Point out Plasmodium parasites and leukocytes.
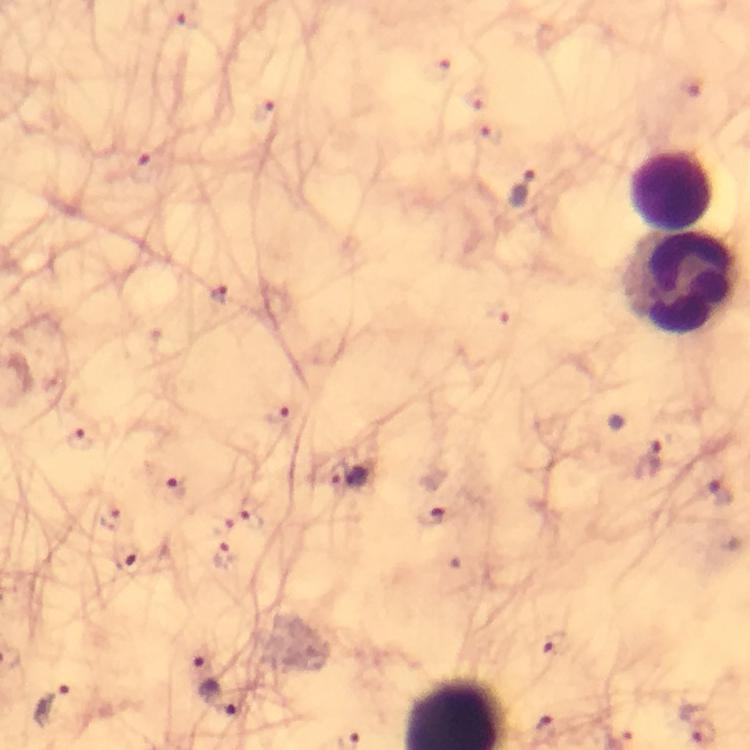
Approximate centers as (x, y) in pixels.
Plasmodium parasites: (440, 70), (692, 86), (478, 100), (262, 113), (493, 132), (140, 168), (522, 188), (218, 295), (280, 419), (79, 440), (651, 459), (333, 475), (356, 480), (173, 488), (716, 494), (250, 515), (431, 517), (109, 518), (221, 526), (230, 555), (127, 561), (546, 644), (201, 657), (222, 701), (52, 706).
Leukocytes: (670, 190), (683, 282).

Summary:
  - Context: from a malaria diagnostic workup
  - Immersion oil: used
  - Image size: 750×750 pixels
  - Stain: Giemsa
  - Preparation: thick blood film
  - Magnification: 100x
  - Capture: smartphone photograph through a microscope
  - Cropped from: one field of view